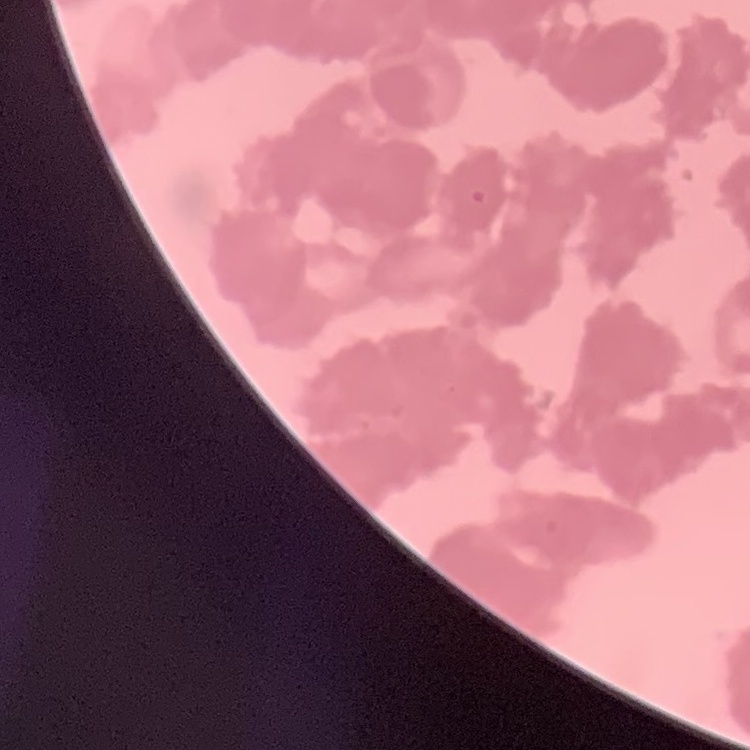
Summary:
  - Red blood cell morphology: rouleaux formation
  - Preparation: thin blood smear
  - Image type: one tile cut from a larger photomicrograph
  - Stain: Field's or Giemsa